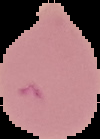

From a thin blood smear. Result: Plasmodium parasites detected. Image is 100×139 pixels. The area outside the segmented cell region is set to black.